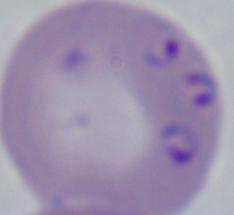
Micrograph. A Babesia parasite is shown. Captured at 1000x magnification.